Classify this cell by malaria status.
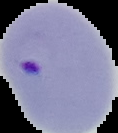

It is parasitized.

image_size: 118×133 pixels
preparation: thin blood film
image_type: segmented cell region with the area outside set to black